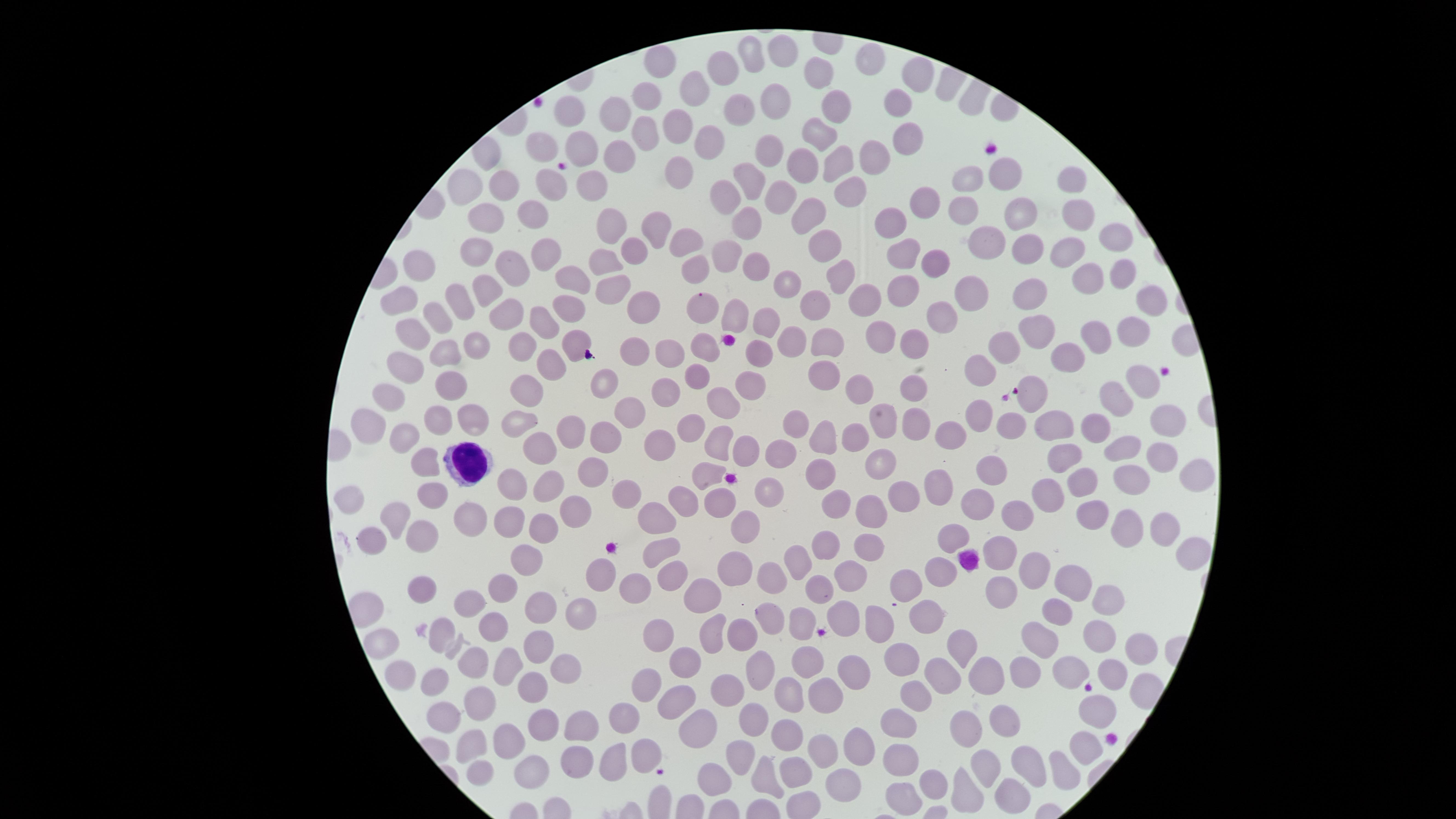
{
  "preparation": "thin blood film",
  "visible_region": "circular",
  "image_size": "1456×819 pixels",
  "capture": "smartphone photograph through the microscope eyepiece",
  "field_of_view": "single",
  "white_blood_cells": "approximate marker points as [x, y] in pixels: [468, 461]",
  "presence": "no malaria parasites identified",
  "stain": "Giemsa",
  "uninfected_red_blood_cells": "approximate marker points as [x, y] in pixels: [782, 48], [747, 54], [660, 62], [870, 62], [726, 64], [816, 74], [920, 74], [696, 87], [647, 92], [771, 98], [895, 104], [840, 109], [741, 110], [615, 114], [571, 118], [681, 119], [820, 132], [640, 136], [905, 136], [710, 138], [548, 144], [578, 146], [770, 149], [616, 155], [873, 156], [841, 158], [803, 166], [686, 167], [750, 177], [506, 179], [1006, 179], [967, 180], [1073, 182], [548, 184], [597, 185], [471, 186], [847, 187], [731, 188], [784, 194], [927, 197], [961, 210], [533, 211], [1074, 211], [813, 212], [1019, 213], [492, 217], [609, 220], [749, 220], [892, 220], [653, 231], [681, 238], [984, 239], [824, 242], [1111, 245], [478, 249], [633, 249], [1032, 249], [906, 250], [541, 251], [727, 253], [1068, 254], [935, 259], [606, 263], [429, 266], [511, 268], [752, 268], [693, 269], [843, 270], [1122, 271], [575, 274], [1089, 278], [904, 281], [786, 286], [613, 290], [1032, 291], [978, 292], [490, 293], [400, 296], [866, 297], [1150, 299], [646, 304], [819, 304], [459, 306], [566, 306], [702, 307], [438, 316], [505, 316], [732, 317], [944, 317], [548, 318], [765, 323], [1131, 326], [416, 327], [1037, 329], [826, 332], [877, 335], [1098, 336], [473, 341], [791, 341], [916, 343], [522, 345], [573, 347], [1003, 347], [705, 348], [445, 349], [759, 353], [636, 354], [1061, 354], [666, 358], [550, 362], [407, 367], [820, 368], [983, 370], [606, 376], [700, 377], [452, 379], [1139, 383], [1035, 385], [524, 386], [753, 386], [915, 386], [857, 388], [666, 392], [397, 397], [1112, 400], [726, 405], [631, 408], [982, 414], [1166, 414], [471, 419], [443, 420], [1056, 421], [519, 423], [1005, 424], [1094, 424], [795, 425], [916, 426], [886, 427], [374, 428], [566, 429], [688, 429], [822, 431], [950, 433], [610, 436], [408, 437], [718, 440], [858, 440], [659, 441], [543, 446], [1121, 448], [749, 450], [782, 450], [1157, 454], [1065, 455], [428, 461], [878, 465], [991, 467], [710, 471], [823, 471], [593, 472], [1200, 473], [1134, 479], [510, 482], [1089, 482], [544, 486], [942, 487], [627, 491], [429, 492], [771, 492], [1053, 493], [902, 494], [351, 496], [681, 498], [835, 500], [977, 500], [722, 502], [577, 506], [877, 507], [396, 514], [1093, 514], [655, 516], [471, 517], [513, 517], [1022, 517], [546, 523], [745, 523], [1162, 527], [1124, 532], [422, 534], [952, 538], [369, 544], [822, 546], [870, 546], [1184, 550], [660, 551], [1003, 554], [529, 555], [802, 558], [734, 563], [938, 567], [1035, 568], [604, 571], [845, 572], [672, 575], [778, 575], [1076, 576], [909, 580], [503, 582], [636, 587], [821, 587], [422, 589], [1108, 591], [1000, 592], [709, 599], [470, 605], [539, 606], [585, 607], [1053, 611], [842, 615], [925, 616], [770, 618], [803, 619], [495, 623], [875, 623], [740, 629], [659, 630], [441, 632], [1099, 632], [1037, 635], [711, 637], [381, 640], [961, 643], [543, 644], [1143, 646], [809, 657], [687, 660], [473, 662], [900, 662], [507, 663], [566, 666], [1020, 668], [754, 670], [1117, 671], [852, 672], [1068, 672], [982, 673], [399, 674], [437, 675], [943, 676], [649, 682], [535, 685], [727, 691], [791, 693], [827, 694], [914, 697], [482, 699], [678, 701], [1096, 705], [443, 712], [625, 720], [547, 722], [703, 722], [899, 722], [998, 722], [753, 723], [582, 726], [961, 729], [789, 735], [504, 737], [474, 742], [1083, 742], [854, 746], [649, 751], [902, 753], [825, 754], [742, 757], [612, 758], [577, 761], [1026, 761], [986, 769], [1062, 769], [482, 772], [530, 772], [792, 774], [709, 776], [765, 776], [841, 780], [932, 784], [962, 788], [906, 792], [1005, 802]"
}